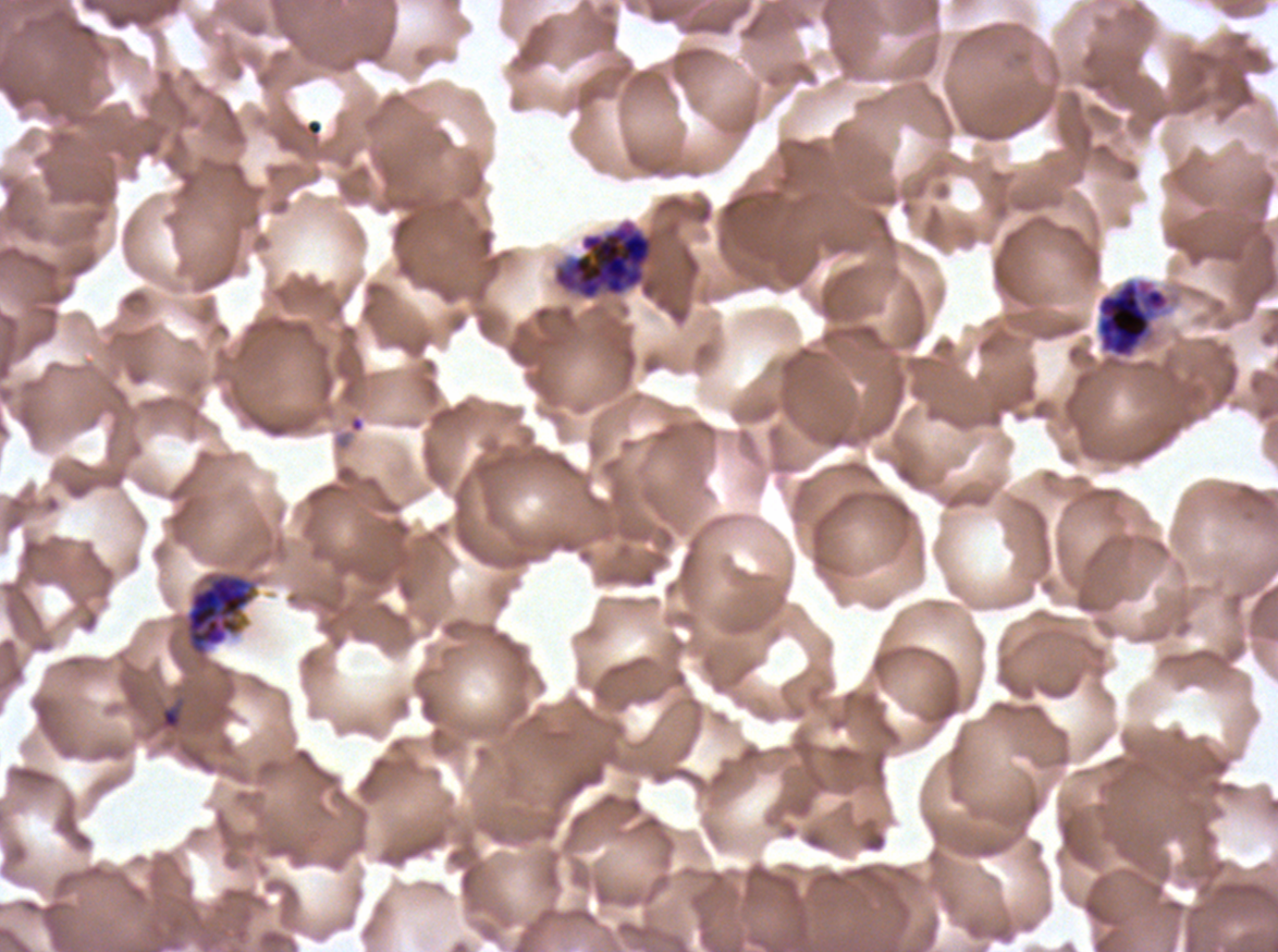 Approximate bounding boxes as [x1, y1, x2, y2] in pixels. Debris locations: [158, 698, 185, 732]. Segmenter locations: [552, 218, 657, 301], [182, 569, 259, 660]. Late schizont locations: [1095, 277, 1172, 360]. Giemsa-stained preparation. Image is 1278×952 pixels. Thin blood film. One sub-image of a larger composite. Life-cycle stages observed: late schizont, segmenter. P. falciparum from a patient in The Gambia, cultured ex vivo for 24 to 48 hours.